Point out each Plasmodium parasite.
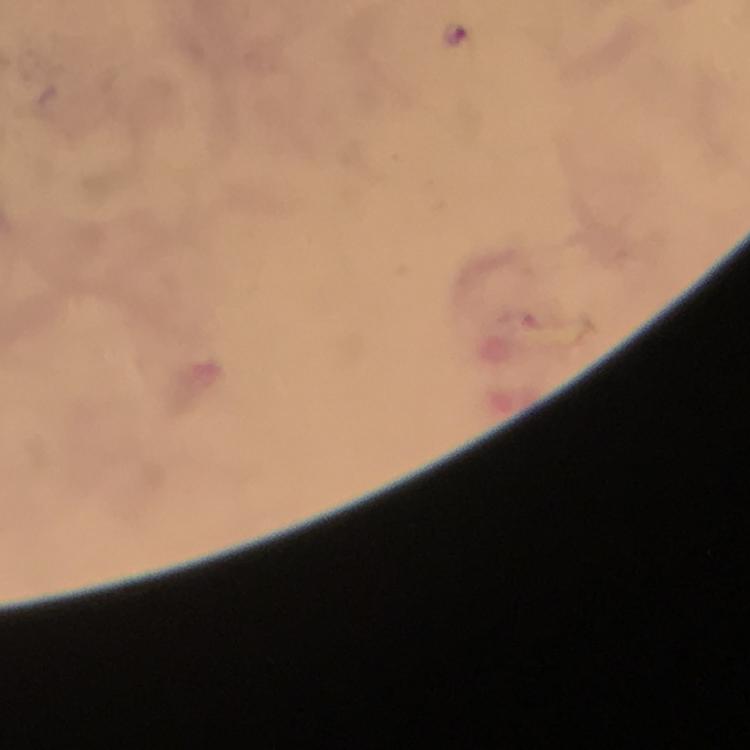
Approximate centers as {x, y} in pixels.
Plasmodium parasites: {456, 33}.

Summary:
  - Image size: 750×750 pixels
  - Context: from a diagnostic examination for malaria
  - Immersion oil: applied
  - Magnification: 100x
  - Preparation: thick smear
  - Stain: Giemsa
  - Capture: smartphone photograph through a microscope
  - Cropped from: one field of view